Locate every malaria parasite and every leukocyte.
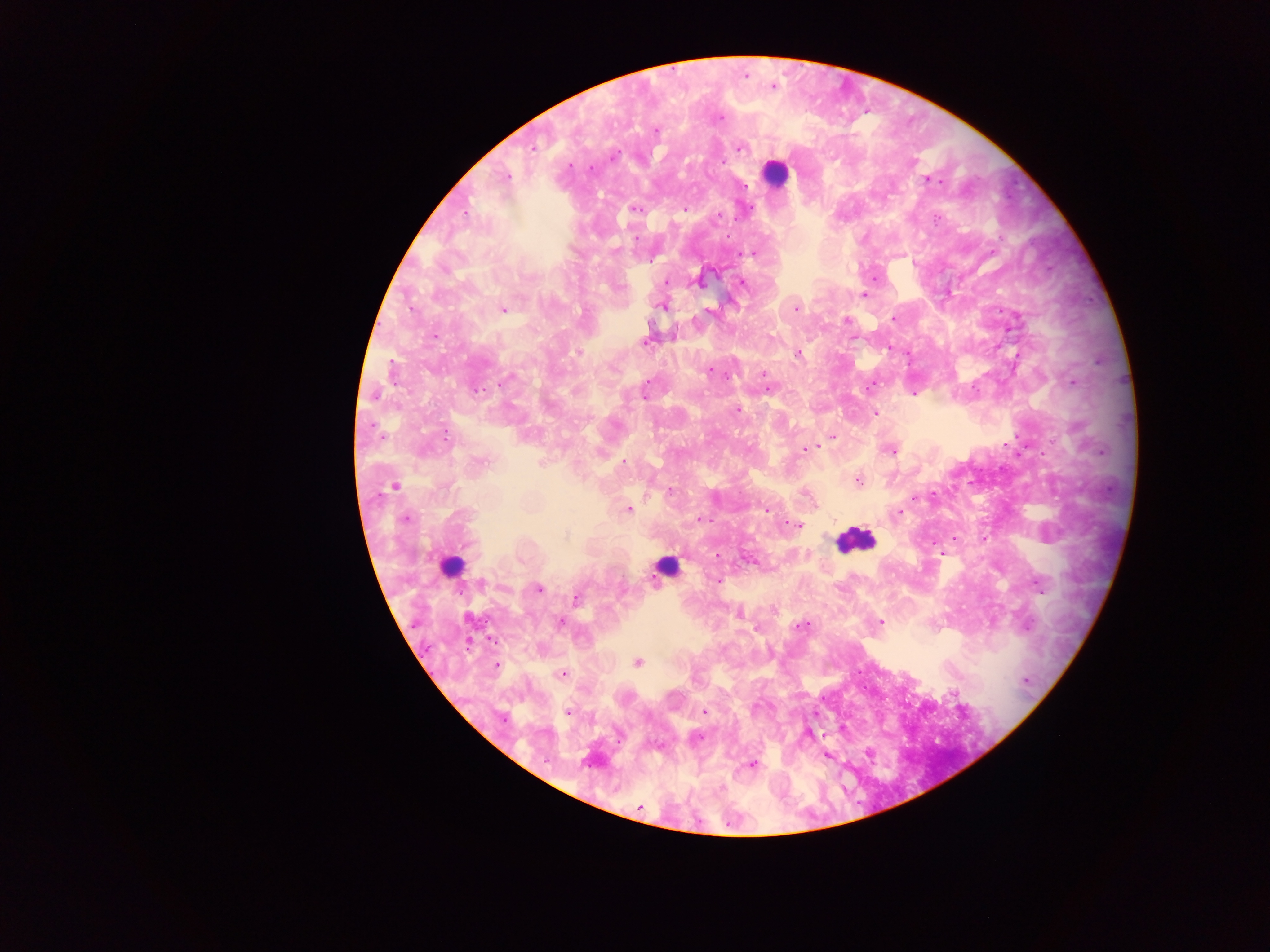

Approximate centers as {x, y} in pixels.
Malaria parasites: {773, 86}, {720, 118}, {655, 130}, {533, 147}, {739, 148}, {614, 156}, {724, 161}, {570, 165}, {590, 168}, {506, 177}, {928, 180}, {936, 182}, {745, 186}, {635, 208}, {684, 209}, {718, 217}, {937, 220}, {636, 239}, {616, 250}, {751, 253}, {875, 278}, {666, 282}, {743, 283}, {864, 294}, {662, 306}, {502, 309}, {796, 309}, {709, 311}, {893, 318}, {847, 320}, {434, 336}, {645, 342}, {578, 352}, {798, 352}, {392, 369}, {710, 372}, {763, 373}, {766, 379}, {1072, 382}, {646, 384}, {871, 386}, {478, 390}, {767, 390}, {914, 394}, {644, 395}, {737, 410}, {874, 413}, {446, 435}, {832, 437}, {824, 440}, {820, 444}, {806, 449}, {891, 450}, {1100, 451}, {482, 461}, {623, 462}, {858, 480}, {395, 486}, {670, 491}, {805, 494}, {915, 498}, {628, 510}, {767, 511}, {899, 513}, {405, 519}, {699, 519}, {798, 525}, {566, 536}, {940, 553}, {718, 555}, {717, 581}, {481, 583}, {538, 588}, {576, 598}, {773, 611}, {740, 615}, {880, 622}, {561, 623}, {801, 627}, {638, 663}, {496, 666}, {563, 674}, {1026, 681}, {754, 707}, {705, 712}, {567, 713}, {698, 739}, {753, 763}, {640, 808}.
Leukocytes: {775, 172}, {854, 539}, {451, 564}, {664, 567}.

Image is 1270×952 pixels. Mobile-phone photograph taken through the microscope. Thick blood smear. Sample from Ghana. Single field of view.